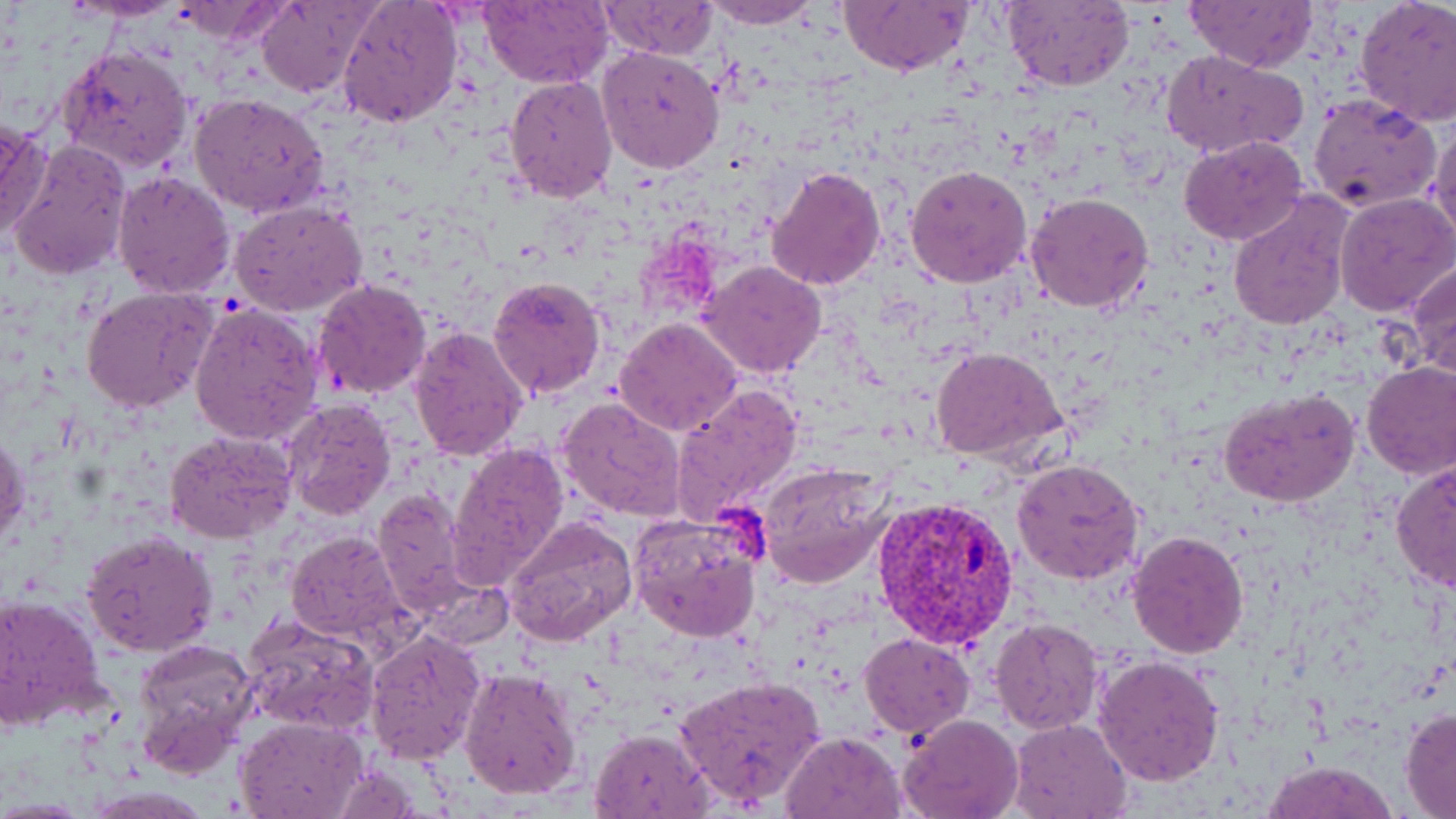
Approximate bounding boxes as (x1, y1, x2, y2) in pixels. Plasmodium vivax-infected red blood cell locations: (870, 492, 1019, 650). Uninfected red blood cell locations: (69, 0, 187, 21), (257, 0, 377, 97), (336, 0, 465, 129), (698, 0, 822, 28), (1185, 0, 1316, 72), (1355, 0, 1456, 126), (477, 1, 612, 85), (598, 1, 719, 59), (838, 1, 971, 76), (1004, 1, 1132, 91), (174, 3, 286, 43), (597, 45, 725, 175), (56, 46, 195, 174), (1162, 48, 1308, 159), (504, 76, 618, 203), (189, 91, 330, 219), (1309, 93, 1442, 211), (0, 118, 51, 240), (1428, 123, 1456, 246), (1179, 135, 1310, 245), (7, 140, 134, 281), (905, 165, 1033, 287), (767, 167, 886, 291), (112, 171, 234, 299), (1025, 191, 1154, 314), (1334, 192, 1456, 315), (1227, 193, 1353, 332), (230, 201, 369, 317), (699, 261, 827, 378), (1409, 261, 1456, 380), (489, 274, 607, 399), (313, 280, 434, 401), (81, 287, 219, 412), (188, 303, 322, 444), (613, 317, 742, 439), (600, 322, 776, 513), (406, 325, 529, 463), (932, 348, 1066, 463), (1362, 362, 1456, 480), (671, 384, 805, 524), (1219, 388, 1359, 508), (557, 397, 686, 521), (281, 398, 396, 519), (164, 429, 297, 546), (1, 431, 28, 550), (450, 440, 569, 585), (1011, 458, 1143, 586), (1390, 460, 1456, 590), (758, 463, 894, 588), (370, 487, 474, 611), (506, 515, 639, 649), (629, 516, 764, 644), (79, 529, 219, 658), (284, 530, 411, 650), (1127, 530, 1248, 659), (0, 595, 107, 731), (242, 614, 378, 735), (991, 617, 1104, 734), (364, 629, 486, 763), (859, 633, 975, 738), (134, 639, 261, 773), (1092, 655, 1224, 788), (458, 666, 581, 800), (675, 676, 828, 809), (1400, 707, 1456, 817), (898, 713, 1022, 819), (234, 714, 366, 818), (1008, 718, 1131, 818), (589, 728, 712, 819), (783, 730, 908, 819), (1261, 760, 1399, 819). Slide-level diagnosis: Plasmodium vivax. 1000x magnification. Thin blood film. One field of a larger specimen. Image is 1456×819 pixels. Optical microscopy. May-Grünwald-Giemsa stain.